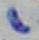
modality = photomicrograph
magnification = 1000x
identification = Toxoplasma gondii